State which cell type is depicted.
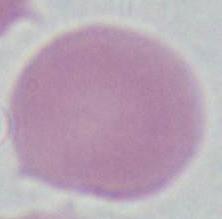

This is an erythrocyte.

Summary:
  - Modality: photomicrograph
  - Magnification: 1000x